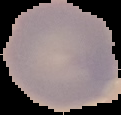
The area outside the segmented cell region is set to black. From a thin blood smear. Image is 121×115 pixels. Malaria status: uninfected.